Assess this cell for malaria.
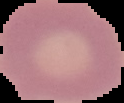

It is uninfected.

preparation = thin blood smear
image size = 124×103 pixels
image type = segmented cell region on a black background